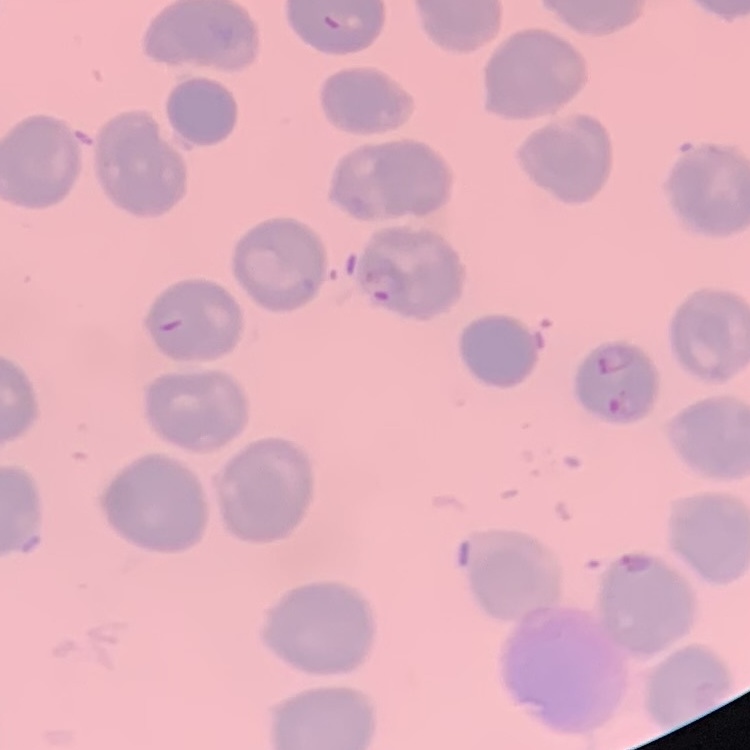

red blood cell morphology = no rouleaux formation
image type = square crop of a larger photomicrograph
preparation = thin peripheral smear
stain = Field's or Giemsa